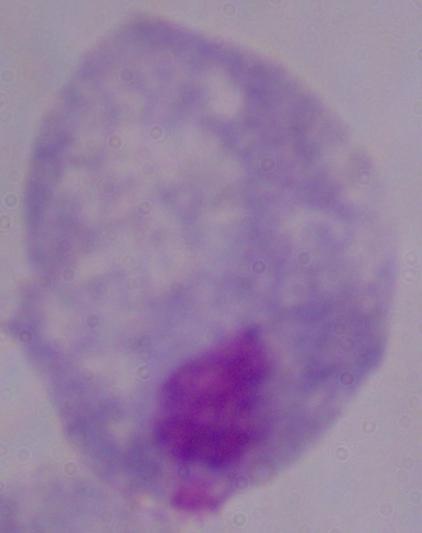
Summary:
  - Modality: micrograph
  - Identification: trichomonad
  - Magnification: 1000x